Identify the blood parasite species.
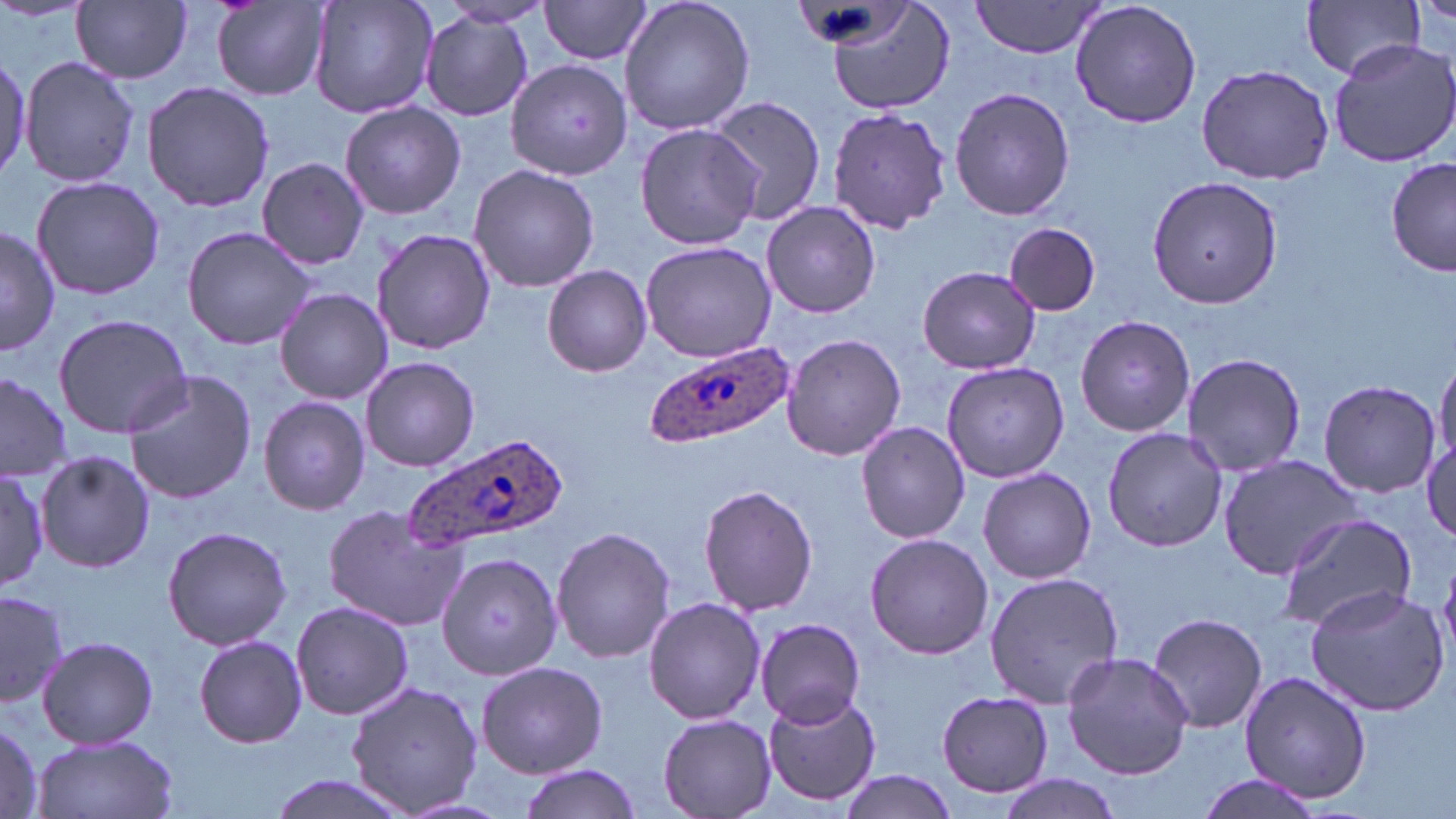
Plasmodium ovale.

Approximate bounding boxes as named x1/y1/x2/y2 corners in pixels. Uninfected red blood cell locations: (x1=306, y1=0, x2=440, y2=120), (x1=539, y1=0, x2=656, y2=65), (x1=618, y1=0, x2=755, y2=135), (x1=822, y1=0, x2=955, y2=113), (x1=1069, y1=0, x2=1204, y2=129), (x1=1301, y1=0, x2=1425, y2=79), (x1=72, y1=1, x2=191, y2=84), (x1=971, y1=1, x2=1104, y2=58), (x1=213, y1=2, x2=330, y2=99), (x1=436, y1=2, x2=554, y2=30), (x1=418, y1=13, x2=535, y2=123), (x1=1327, y1=39, x2=1456, y2=170), (x1=0, y1=51, x2=29, y2=186), (x1=20, y1=56, x2=141, y2=189), (x1=505, y1=58, x2=634, y2=182), (x1=1195, y1=64, x2=1336, y2=184), (x1=141, y1=80, x2=275, y2=212), (x1=949, y1=86, x2=1075, y2=222), (x1=705, y1=94, x2=828, y2=225), (x1=340, y1=101, x2=466, y2=219), (x1=825, y1=104, x2=953, y2=236), (x1=635, y1=123, x2=766, y2=250), (x1=257, y1=157, x2=370, y2=270), (x1=1387, y1=159, x2=1455, y2=278), (x1=468, y1=163, x2=599, y2=293), (x1=1146, y1=174, x2=1284, y2=309), (x1=30, y1=175, x2=165, y2=300), (x1=761, y1=200, x2=881, y2=318), (x1=1004, y1=223, x2=1101, y2=315), (x1=0, y1=226, x2=60, y2=356), (x1=181, y1=227, x2=318, y2=351), (x1=371, y1=228, x2=496, y2=354), (x1=641, y1=241, x2=775, y2=361), (x1=542, y1=265, x2=652, y2=377), (x1=917, y1=265, x2=1042, y2=375), (x1=274, y1=288, x2=394, y2=404), (x1=54, y1=313, x2=193, y2=437), (x1=1075, y1=314, x2=1196, y2=437), (x1=781, y1=333, x2=906, y2=462), (x1=1182, y1=352, x2=1306, y2=478), (x1=360, y1=356, x2=479, y2=472), (x1=1434, y1=356, x2=1455, y2=474), (x1=941, y1=360, x2=1069, y2=483), (x1=0, y1=369, x2=72, y2=483), (x1=123, y1=370, x2=259, y2=505), (x1=1317, y1=379, x2=1441, y2=497), (x1=259, y1=396, x2=371, y2=516), (x1=856, y1=421, x2=973, y2=544), (x1=1101, y1=426, x2=1227, y2=552), (x1=1421, y1=437, x2=1456, y2=544), (x1=35, y1=449, x2=155, y2=574), (x1=1219, y1=454, x2=1360, y2=577), (x1=977, y1=468, x2=1098, y2=584), (x1=0, y1=470, x2=49, y2=589), (x1=698, y1=483, x2=819, y2=616), (x1=323, y1=504, x2=466, y2=630), (x1=1275, y1=513, x2=1417, y2=632), (x1=161, y1=526, x2=292, y2=650), (x1=552, y1=526, x2=676, y2=665), (x1=865, y1=533, x2=993, y2=660), (x1=438, y1=550, x2=562, y2=679), (x1=1440, y1=564, x2=1456, y2=662), (x1=984, y1=570, x2=1124, y2=707), (x1=1304, y1=585, x2=1449, y2=716), (x1=0, y1=589, x2=68, y2=709), (x1=643, y1=597, x2=766, y2=724), (x1=290, y1=600, x2=414, y2=720), (x1=1147, y1=611, x2=1269, y2=734), (x1=756, y1=618, x2=869, y2=726), (x1=37, y1=634, x2=159, y2=749), (x1=193, y1=634, x2=307, y2=748), (x1=1062, y1=651, x2=1194, y2=779), (x1=475, y1=660, x2=608, y2=777), (x1=1236, y1=671, x2=1376, y2=804), (x1=344, y1=680, x2=483, y2=816), (x1=764, y1=689, x2=882, y2=805), (x1=936, y1=690, x2=1055, y2=797), (x1=658, y1=714, x2=775, y2=816), (x1=0, y1=719, x2=44, y2=818), (x1=31, y1=733, x2=179, y2=819), (x1=519, y1=765, x2=641, y2=819), (x1=836, y1=771, x2=960, y2=817), (x1=263, y1=774, x2=416, y2=819), (x1=997, y1=774, x2=1127, y2=818), (x1=1190, y1=775, x2=1326, y2=819). Plasmodium ovale-infected red blood cell locations: (x1=648, y1=339, x2=795, y2=448), (x1=401, y1=432, x2=564, y2=552). Image is 1456×819 pixels. May-Grünwald-Giemsa-stained preparation. Thin blood smear. One field of a larger specimen. Light microscopy. Captured at 1000x magnification.